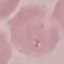

Summary:
  - Malaria status: uninfected
  - Stain: Giemsa
  - Image type: automatically extracted cell patch, resized to 64 × 64 pixels
  - Preparation: thin blood film
  - Capture: smartphone through the microscope eyepiece